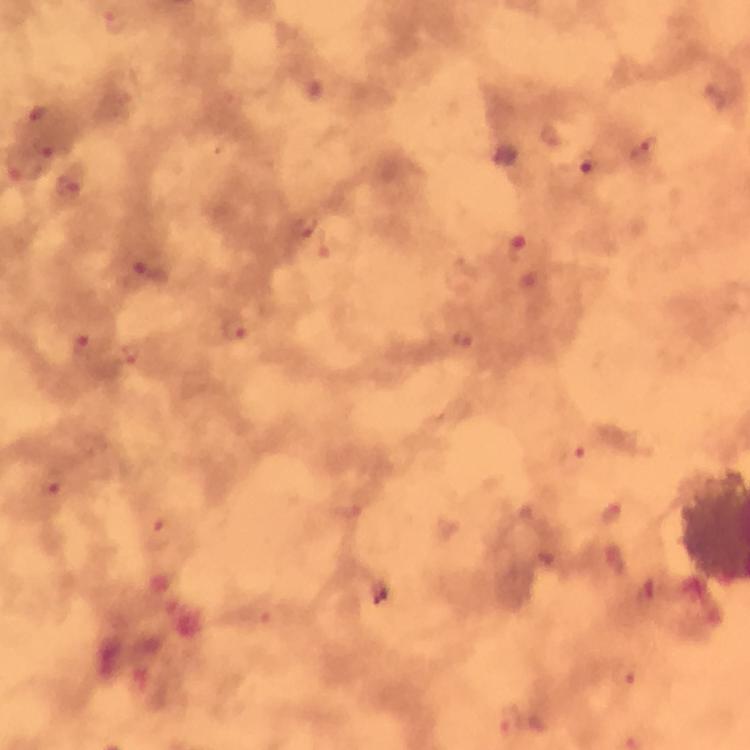

Approximate centers as [x, y] in pixels.
Summary:
  - Malaria parasite locations: [117, 24], [46, 148], [645, 150], [584, 164], [18, 166], [70, 186], [307, 226], [516, 245], [142, 276], [233, 328], [464, 339], [80, 348], [127, 353], [571, 458], [51, 484], [162, 535], [623, 677], [511, 721]
  - Context: from a diagnostic examination for malaria
  - Stain: Giemsa
  - Magnification: 100x
  - Immersion oil: used
  - Image size: 750×750 pixels
  - Cropped from: one field of view
  - Preparation: thick blood film
  - Capture: smartphone camera through the microscope